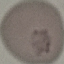 Result: negative for malaria parasites. Cell patch, automatically extracted from a larger field of view and resized to 64 × 64 pixels. Giemsa-stained preparation. Thin blood film. Photographed with a smartphone camera at the microscope eyepiece.